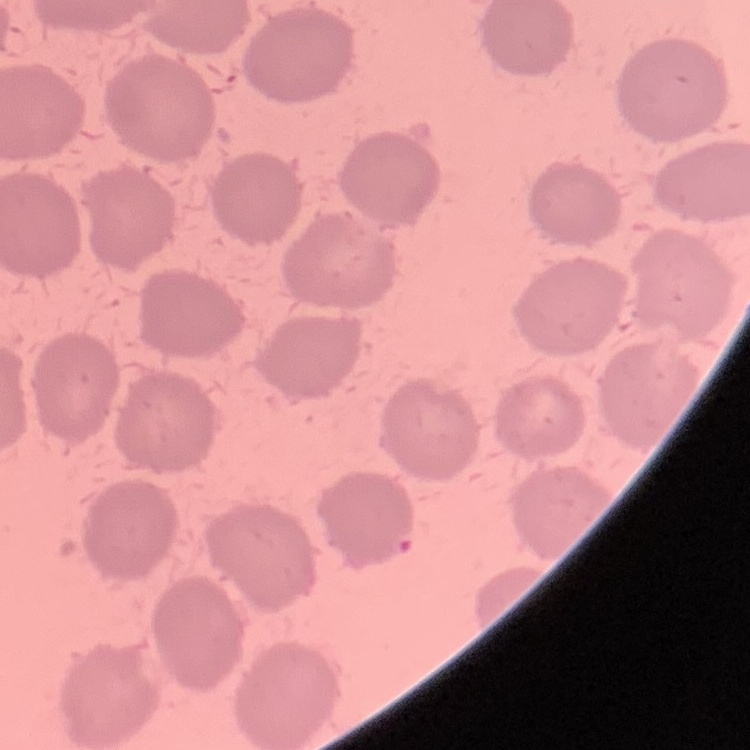
red_blood_cell_morphology: no rouleaux formation
stain: Field's or Giemsa
image_type: square crop of a larger photomicrograph
preparation: thin blood smear